Evaluate for Plasmodium parasites.
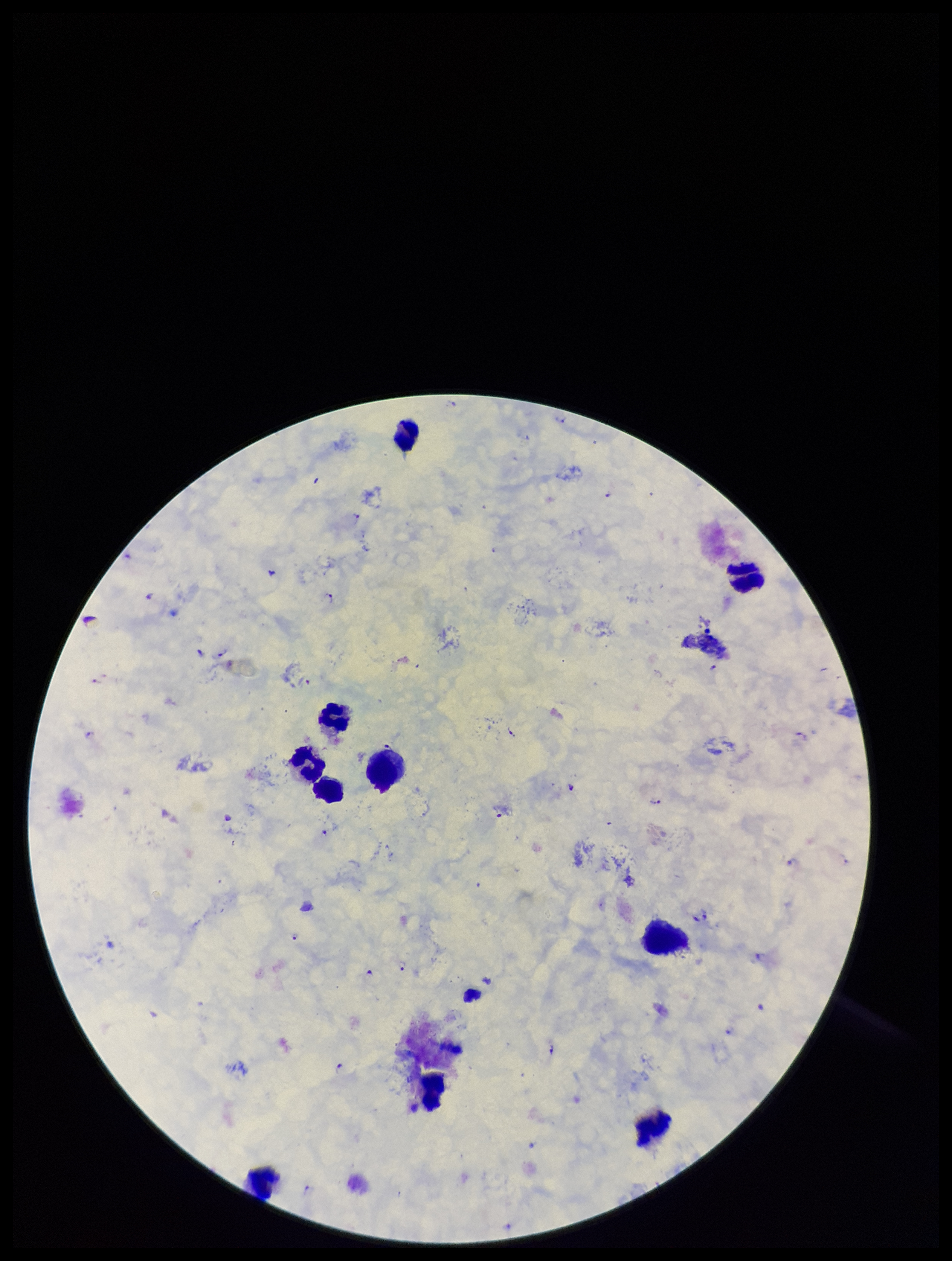
Seen.

parasite count = 25
preparation = thick smear
leukocyte count = 10
capture = smartphone photograph through the microscope eyepiece
patient malaria status = positive
stain = Giemsa
field of view = one from this slide
species reported for this patient = Plasmodium falciparum
image size = 952×1261 pixels